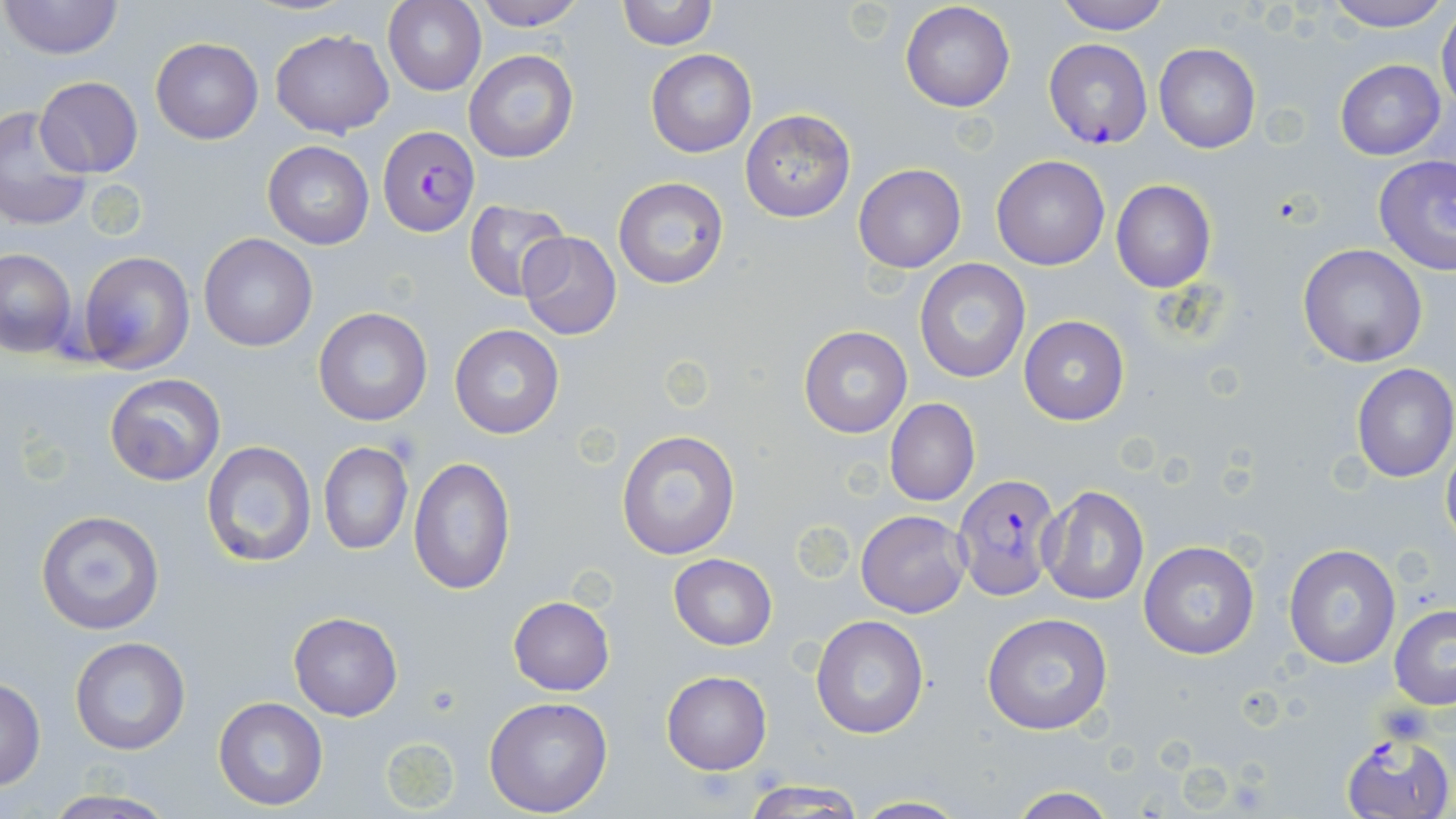

Approximate bounding boxes as [x1, y1, x2, y2] in pixels. Plasmodium falciparum-infected red blood cell locations: [1043, 37, 1152, 148], [376, 126, 480, 237], [951, 473, 1062, 600], [1340, 732, 1455, 819]. Uninfected red blood cell locations: [1, 0, 123, 61], [475, 0, 584, 29], [617, 0, 721, 49], [1054, 0, 1170, 34], [1322, 0, 1456, 32], [383, 1, 485, 96], [899, 1, 1015, 113], [1436, 10, 1456, 113], [270, 28, 395, 138], [151, 37, 262, 145], [1153, 43, 1259, 154], [462, 49, 579, 164], [647, 50, 756, 157], [1335, 58, 1445, 159], [35, 76, 142, 178], [0, 105, 92, 230], [740, 109, 855, 224], [263, 140, 374, 250], [1374, 155, 1456, 275], [992, 156, 1110, 270], [853, 164, 966, 274], [612, 176, 730, 290], [1111, 179, 1217, 293], [463, 199, 569, 300], [516, 231, 621, 341], [200, 233, 317, 352], [1298, 243, 1428, 368], [1, 248, 76, 358], [77, 251, 194, 374], [914, 260, 1032, 384], [313, 307, 432, 425], [1019, 316, 1129, 425], [450, 324, 563, 439], [799, 325, 912, 439], [1350, 362, 1456, 483], [104, 373, 224, 485], [884, 397, 979, 507], [616, 431, 740, 559], [1441, 438, 1456, 551], [201, 440, 318, 569], [318, 441, 413, 555], [409, 457, 514, 594], [1039, 485, 1150, 606], [34, 510, 164, 635], [856, 510, 970, 618], [1138, 540, 1259, 660], [1282, 543, 1401, 669], [669, 554, 777, 651], [508, 596, 615, 695], [1389, 604, 1456, 709], [289, 611, 402, 720], [982, 612, 1113, 737], [809, 614, 928, 740], [69, 637, 191, 756], [662, 670, 772, 775], [0, 676, 47, 790], [213, 696, 328, 811], [484, 696, 613, 817], [380, 734, 464, 815], [742, 779, 866, 818], [1005, 787, 1120, 819], [39, 791, 182, 819], [851, 795, 969, 817]. Slide-level diagnosis: Plasmodium falciparum. Light microscopy. One field of a larger specimen. May-Grünwald-Giemsa-stained preparation. Captured at 1000x magnification. Thin blood smear. Image is 1456×819 pixels.